State which parasite is depicted.
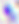

This is Toxoplasma gondii.

modality = photomicrograph
magnification = 400x